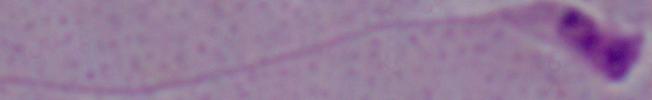

1000x magnification. Micrograph. A Leishmania parasite is shown.